Outline each blood parasite and name the species.
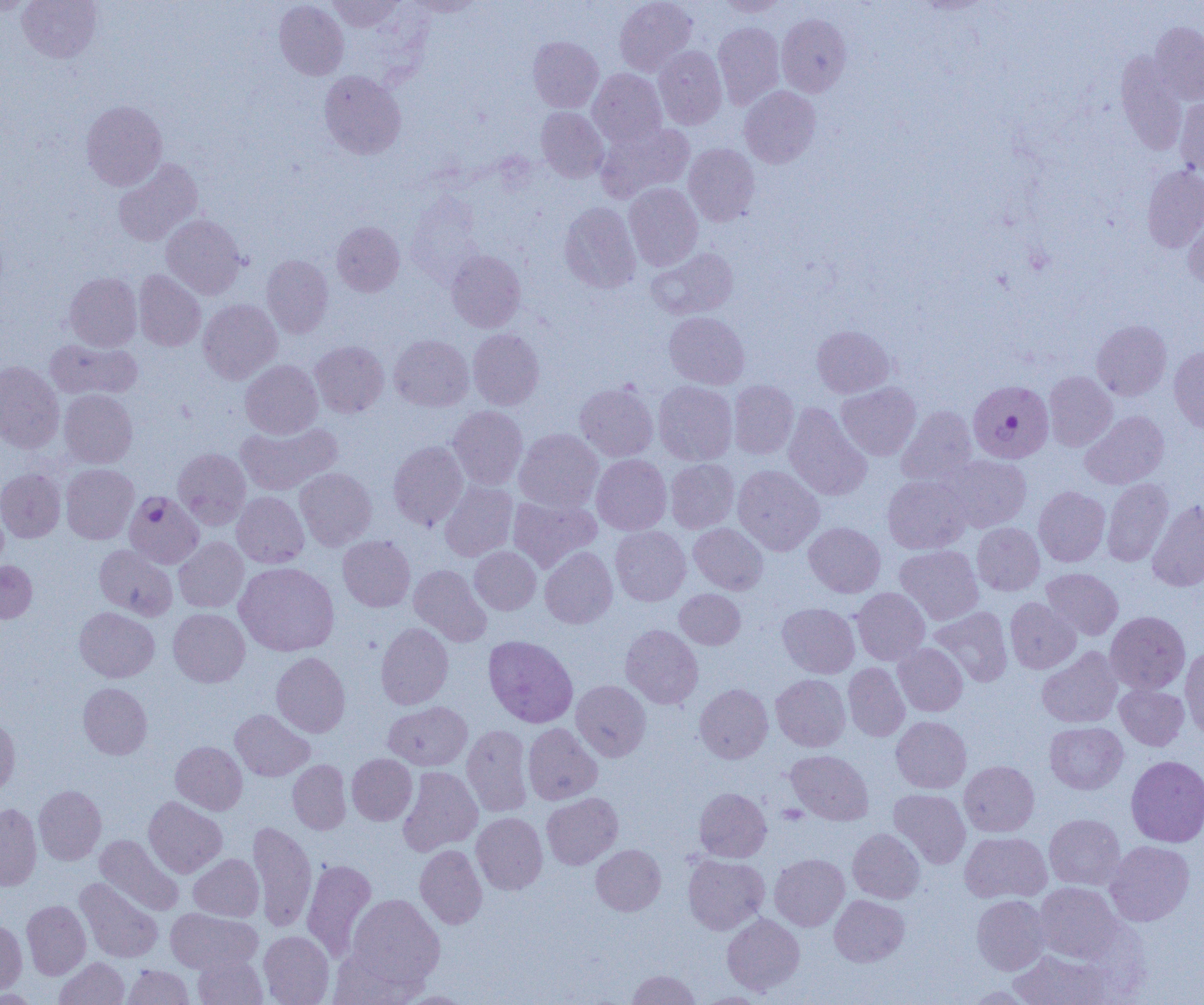
Approximate bounding boxes as named x1/y1/x2/y2 corners in pixels.
Plasmodium falciparum-infected red blood cells: (x1=965, y1=382, x2=1050, y2=464), (x1=124, y1=491, x2=203, y2=569).
No Plasmodium ovale, Plasmodium malariae, Plasmodium vivax, Babesia divergens, or Trypanosoma brucei observed.

Summary:
  - Uninfected red blood cell locations: (x1=18, y1=0, x2=102, y2=62), (x1=326, y1=0, x2=403, y2=31), (x1=408, y1=0, x2=485, y2=17), (x1=615, y1=0, x2=696, y2=76), (x1=716, y1=0, x2=787, y2=16), (x1=0, y1=1, x2=37, y2=16), (x1=274, y1=1, x2=349, y2=80), (x1=777, y1=13, x2=851, y2=96), (x1=1150, y1=21, x2=1204, y2=105), (x1=713, y1=22, x2=785, y2=108), (x1=528, y1=36, x2=603, y2=112), (x1=654, y1=46, x2=727, y2=129), (x1=1114, y1=53, x2=1187, y2=155), (x1=588, y1=69, x2=667, y2=147), (x1=319, y1=70, x2=406, y2=159), (x1=740, y1=86, x2=821, y2=168), (x1=1175, y1=97, x2=1204, y2=178), (x1=81, y1=100, x2=167, y2=190), (x1=536, y1=107, x2=609, y2=182), (x1=596, y1=122, x2=695, y2=201), (x1=683, y1=143, x2=760, y2=225), (x1=113, y1=158, x2=203, y2=246), (x1=1142, y1=165, x2=1204, y2=252), (x1=624, y1=183, x2=702, y2=270), (x1=559, y1=202, x2=640, y2=293), (x1=1184, y1=210, x2=1204, y2=290), (x1=161, y1=214, x2=246, y2=299), (x1=332, y1=221, x2=405, y2=296), (x1=648, y1=248, x2=739, y2=319), (x1=446, y1=250, x2=526, y2=332), (x1=261, y1=254, x2=333, y2=337), (x1=134, y1=270, x2=205, y2=351), (x1=65, y1=272, x2=142, y2=351), (x1=199, y1=299, x2=282, y2=383), (x1=664, y1=312, x2=749, y2=389), (x1=1091, y1=319, x2=1171, y2=400), (x1=812, y1=325, x2=894, y2=397), (x1=468, y1=329, x2=544, y2=409), (x1=389, y1=335, x2=474, y2=411), (x1=44, y1=338, x2=142, y2=400), (x1=310, y1=341, x2=388, y2=417), (x1=1169, y1=345, x2=1204, y2=435), (x1=240, y1=360, x2=322, y2=439), (x1=0, y1=361, x2=64, y2=452), (x1=1044, y1=371, x2=1117, y2=451), (x1=728, y1=380, x2=799, y2=459), (x1=654, y1=381, x2=738, y2=465), (x1=575, y1=382, x2=658, y2=461), (x1=836, y1=382, x2=921, y2=460), (x1=60, y1=389, x2=137, y2=467), (x1=783, y1=403, x2=872, y2=501), (x1=448, y1=405, x2=528, y2=489), (x1=896, y1=405, x2=978, y2=486), (x1=1080, y1=411, x2=1169, y2=489), (x1=236, y1=422, x2=341, y2=495), (x1=514, y1=428, x2=603, y2=512), (x1=388, y1=441, x2=468, y2=530), (x1=173, y1=448, x2=250, y2=529), (x1=592, y1=454, x2=671, y2=535), (x1=942, y1=454, x2=1031, y2=532), (x1=665, y1=458, x2=739, y2=533), (x1=61, y1=464, x2=138, y2=544), (x1=733, y1=465, x2=824, y2=555), (x1=0, y1=468, x2=65, y2=542), (x1=295, y1=468, x2=377, y2=550), (x1=883, y1=475, x2=971, y2=554), (x1=1102, y1=478, x2=1173, y2=566), (x1=439, y1=481, x2=518, y2=561), (x1=1034, y1=486, x2=1110, y2=566), (x1=232, y1=492, x2=309, y2=568), (x1=509, y1=495, x2=601, y2=572), (x1=1147, y1=499, x2=1204, y2=591), (x1=804, y1=522, x2=885, y2=597), (x1=972, y1=522, x2=1045, y2=596), (x1=689, y1=523, x2=768, y2=594), (x1=610, y1=525, x2=691, y2=606), (x1=338, y1=535, x2=415, y2=611), (x1=174, y1=537, x2=248, y2=612), (x1=95, y1=544, x2=177, y2=620), (x1=469, y1=546, x2=541, y2=614), (x1=540, y1=546, x2=617, y2=628), (x1=894, y1=546, x2=983, y2=625), (x1=0, y1=560, x2=37, y2=623), (x1=234, y1=562, x2=339, y2=656), (x1=409, y1=564, x2=490, y2=646), (x1=1042, y1=568, x2=1123, y2=640), (x1=851, y1=587, x2=929, y2=665), (x1=674, y1=589, x2=745, y2=649), (x1=1005, y1=598, x2=1080, y2=673), (x1=778, y1=603, x2=859, y2=678), (x1=930, y1=606, x2=1012, y2=686), (x1=74, y1=607, x2=159, y2=682), (x1=168, y1=608, x2=249, y2=686), (x1=1105, y1=611, x2=1190, y2=693), (x1=376, y1=622, x2=453, y2=709), (x1=620, y1=625, x2=703, y2=709), (x1=483, y1=635, x2=578, y2=727), (x1=893, y1=643, x2=968, y2=716), (x1=1180, y1=646, x2=1204, y2=740), (x1=1037, y1=647, x2=1122, y2=728), (x1=271, y1=652, x2=350, y2=737), (x1=843, y1=663, x2=910, y2=741), (x1=771, y1=674, x2=850, y2=751), (x1=571, y1=680, x2=650, y2=761), (x1=78, y1=682, x2=152, y2=759), (x1=695, y1=683, x2=773, y2=763), (x1=1115, y1=684, x2=1189, y2=750), (x1=383, y1=701, x2=472, y2=770), (x1=230, y1=709, x2=314, y2=781), (x1=0, y1=716, x2=20, y2=797), (x1=891, y1=716, x2=971, y2=793), (x1=1045, y1=722, x2=1128, y2=794), (x1=523, y1=723, x2=602, y2=805), (x1=462, y1=724, x2=533, y2=817), (x1=171, y1=741, x2=247, y2=814), (x1=785, y1=750, x2=873, y2=824), (x1=347, y1=753, x2=417, y2=825), (x1=1126, y1=755, x2=1204, y2=847), (x1=287, y1=760, x2=351, y2=834), (x1=959, y1=760, x2=1039, y2=836), (x1=398, y1=766, x2=482, y2=855), (x1=34, y1=785, x2=106, y2=865), (x1=694, y1=787, x2=771, y2=862), (x1=889, y1=789, x2=971, y2=868), (x1=542, y1=793, x2=623, y2=869), (x1=144, y1=796, x2=227, y2=878), (x1=0, y1=803, x2=41, y2=890), (x1=471, y1=812, x2=548, y2=894), (x1=1044, y1=814, x2=1125, y2=890), (x1=248, y1=821, x2=316, y2=932), (x1=848, y1=828, x2=925, y2=903), (x1=960, y1=831, x2=1052, y2=903), (x1=95, y1=834, x2=183, y2=915), (x1=1104, y1=841, x2=1194, y2=926), (x1=415, y1=844, x2=487, y2=929), (x1=590, y1=844, x2=665, y2=916), (x1=188, y1=853, x2=263, y2=921), (x1=770, y1=853, x2=849, y2=930), (x1=683, y1=854, x2=769, y2=934), (x1=301, y1=859, x2=376, y2=962), (x1=75, y1=878, x2=163, y2=963), (x1=1035, y1=882, x2=1123, y2=963), (x1=347, y1=894, x2=445, y2=988), (x1=829, y1=895, x2=909, y2=966), (x1=972, y1=895, x2=1050, y2=974), (x1=22, y1=900, x2=90, y2=979), (x1=165, y1=908, x2=262, y2=973), (x1=722, y1=913, x2=805, y2=995), (x1=0, y1=920, x2=27, y2=997), (x1=259, y1=931, x2=334, y2=1005), (x1=327, y1=947, x2=422, y2=1005), (x1=1010, y1=949, x2=1113, y2=1005), (x1=193, y1=953, x2=267, y2=1005), (x1=54, y1=958, x2=129, y2=1005), (x1=122, y1=965, x2=193, y2=1004), (x1=626, y1=969, x2=701, y2=1004), (x1=963, y1=986, x2=1038, y2=1004), (x1=393, y1=990, x2=475, y2=1004), (x1=692, y1=992, x2=775, y2=1004)
  - Slide-level diagnosis: Plasmodium falciparum
  - Field of view: one of a larger specimen
  - Modality: optical microscopy
  - Image size: 1204×1005 pixels
  - Magnification: 1000x
  - Preparation: thin blood smear